Identify the blood parasite species.
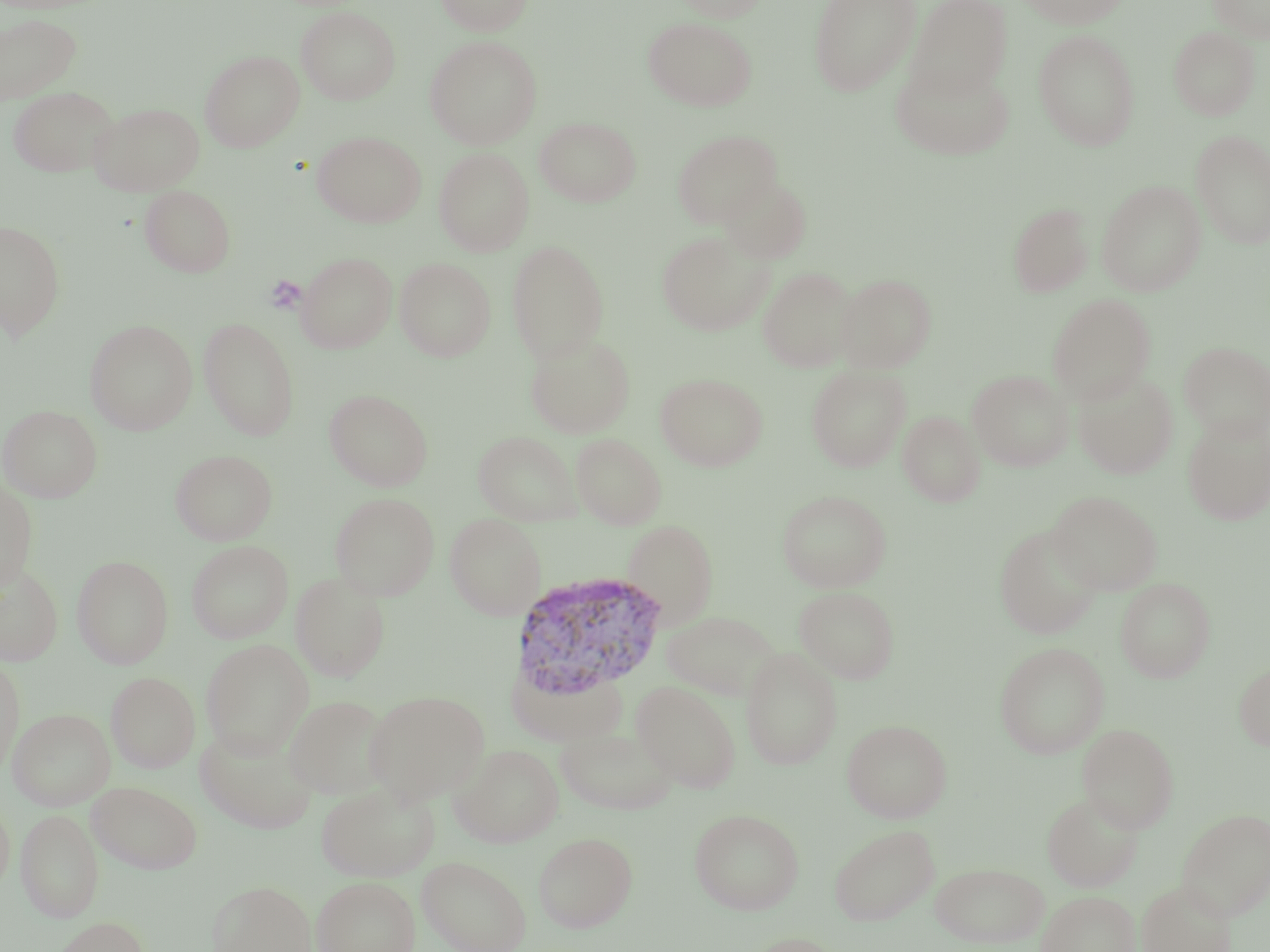
Plasmodium vivax.

uninfected red blood cell locations = approximate bounding boxes as (x1, y1, x2, y2) in pixels: (434, 0, 534, 35), (673, 0, 770, 22), (808, 0, 921, 95), (906, 0, 1013, 99), (1018, 0, 1130, 29), (1207, 0, 1270, 43), (295, 6, 401, 104), (0, 14, 82, 103), (643, 16, 757, 111), (1168, 26, 1260, 121), (1033, 29, 1141, 150), (424, 35, 542, 149), (200, 50, 304, 152), (890, 58, 1015, 160), (7, 85, 119, 178), (89, 101, 205, 196), (534, 116, 641, 208), (672, 129, 783, 228), (1190, 129, 1270, 249), (312, 130, 426, 228), (433, 147, 535, 256), (719, 175, 812, 264), (1097, 179, 1206, 296), (140, 184, 237, 278), (1007, 202, 1094, 298), (0, 220, 66, 341), (657, 229, 773, 336), (506, 240, 610, 363), (296, 251, 397, 353), (395, 258, 496, 362), (759, 266, 857, 372), (836, 273, 937, 372), (1047, 293, 1156, 404), (198, 317, 300, 440), (85, 319, 198, 435), (525, 332, 636, 438), (1179, 341, 1270, 441), (806, 365, 911, 472), (1072, 369, 1179, 479), (968, 370, 1074, 471), (655, 372, 768, 472), (324, 388, 434, 491), (0, 404, 102, 503), (897, 409, 986, 507), (1182, 414, 1270, 526), (473, 430, 582, 526), (570, 433, 667, 529), (170, 449, 278, 545), (0, 479, 38, 591), (777, 489, 891, 592), (1048, 490, 1162, 595), (330, 492, 440, 600), (445, 513, 547, 619), (623, 519, 719, 626), (993, 524, 1104, 639), (186, 540, 293, 643), (71, 555, 173, 669), (0, 562, 63, 666), (290, 572, 391, 682), (1115, 577, 1216, 683), (794, 585, 900, 684), (662, 610, 782, 704), (200, 639, 313, 757), (994, 642, 1110, 759), (739, 648, 843, 770), (0, 656, 24, 776), (1234, 661, 1270, 751), (508, 664, 627, 746), (106, 671, 200, 773), (632, 681, 741, 793), (365, 691, 489, 805), (284, 695, 393, 800), (7, 708, 115, 811), (842, 719, 952, 823), (1077, 723, 1179, 833), (195, 726, 318, 833), (555, 726, 677, 815), (450, 743, 564, 847), (86, 780, 203, 874), (316, 782, 439, 881), (1042, 791, 1144, 891), (0, 799, 14, 895), (16, 808, 103, 923), (689, 808, 804, 914), (1176, 808, 1270, 919), (828, 823, 940, 925), (532, 832, 637, 933), (416, 855, 531, 952), (930, 862, 1050, 948), (311, 875, 420, 952), (207, 879, 317, 952), (1136, 880, 1237, 952), (1036, 890, 1140, 952), (48, 916, 152, 952), (740, 932, 847, 952)
Plasmodium vivax-infected red blood cell locations = approximate bounding boxes as (x1, y1, x2, y2) in pixels: (508, 570, 670, 703)
field of view = single
modality = optical microscopy
stain = May-Grünwald-Giemsa
magnification = 1000x
image size = 1270×952 pixels
preparation = thin blood film